Name the parasite shown.
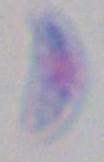
Toxoplasma gondii.

magnification = 1000x
modality = photomicrograph